Classify this cell by malaria status.
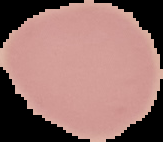

Uninfected.

image type = segmented cell region on a black background
image size = 163×142 pixels
preparation = thin blood film